Identify the parasite.
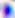

Toxoplasma gondii.

{
  "magnification": "400x",
  "modality": "micrograph"
}